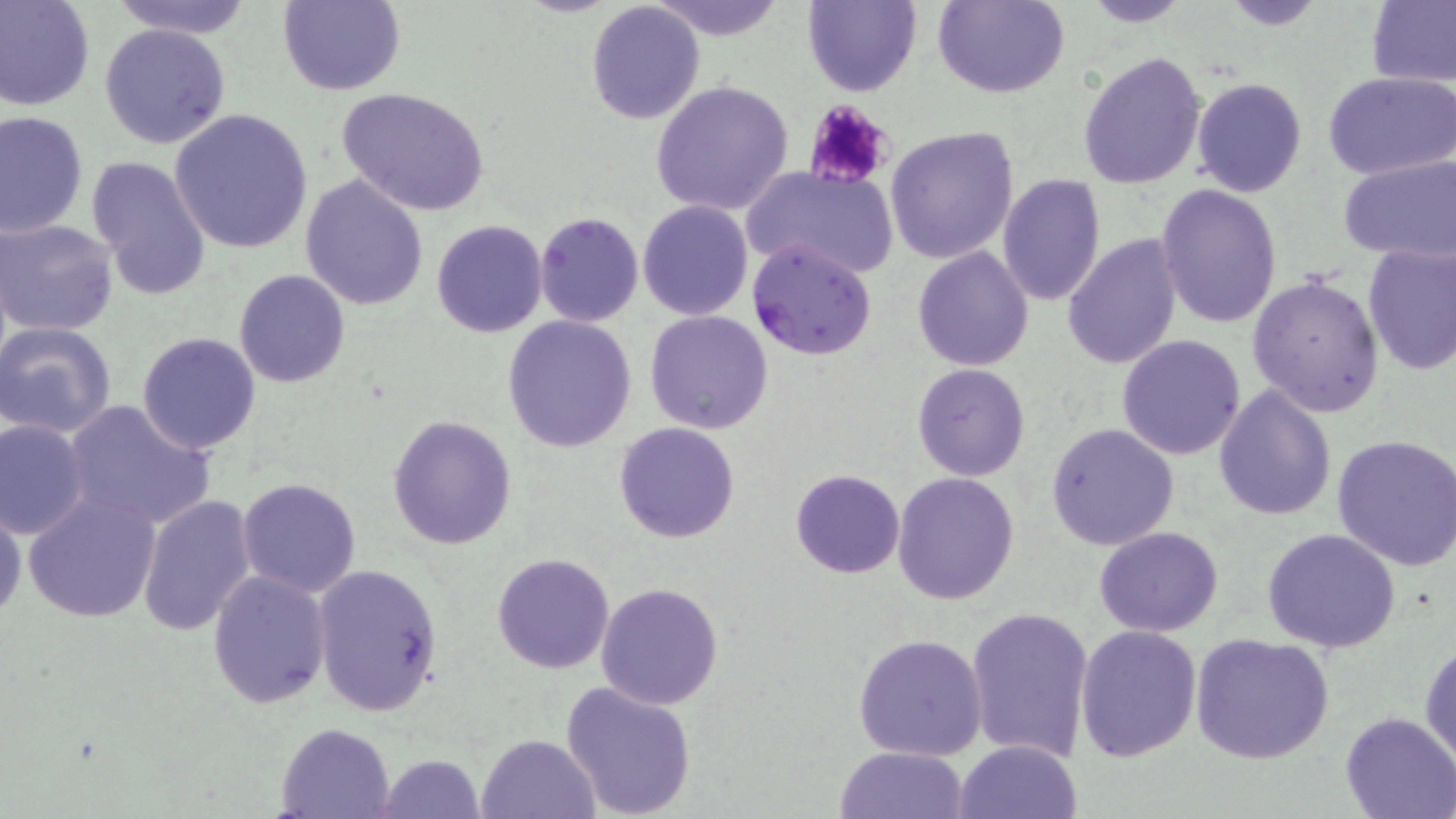

slide-level diagnosis = Plasmodium falciparum
stain = May-Grünwald-Giemsa
Plasmodium falciparum-infected red blood cell locations = approximate bounding boxes as named x1/y1/x2/y2 corners in pixels: (x1=746, y1=236, x2=877, y2=361)
modality = optical microscopy
preparation = thin blood smear
field of view = one of a larger specimen
uninfected red blood cell locations = approximate bounding boxes as named x1/y1/x2/y2 corners in pixels: (x1=0, y1=0, x2=96, y2=112), (x1=105, y1=0, x2=257, y2=38), (x1=275, y1=0, x2=405, y2=95), (x1=647, y1=0, x2=788, y2=40), (x1=934, y1=0, x2=1068, y2=98), (x1=1218, y1=0, x2=1332, y2=29), (x1=1367, y1=0, x2=1456, y2=88), (x1=802, y1=1, x2=921, y2=96), (x1=1078, y1=1, x2=1194, y2=27), (x1=586, y1=2, x2=706, y2=123), (x1=100, y1=23, x2=230, y2=149), (x1=1077, y1=51, x2=1207, y2=189), (x1=1323, y1=72, x2=1456, y2=180), (x1=1191, y1=77, x2=1307, y2=197), (x1=650, y1=79, x2=795, y2=216), (x1=336, y1=87, x2=490, y2=216), (x1=170, y1=108, x2=313, y2=253), (x1=1, y1=111, x2=88, y2=239), (x1=884, y1=126, x2=1019, y2=265), (x1=87, y1=155, x2=212, y2=299), (x1=1337, y1=155, x2=1456, y2=263), (x1=742, y1=166, x2=897, y2=277), (x1=996, y1=172, x2=1106, y2=306), (x1=300, y1=174, x2=430, y2=311), (x1=1155, y1=183, x2=1282, y2=328), (x1=638, y1=200, x2=753, y2=319), (x1=534, y1=212, x2=645, y2=327), (x1=2, y1=217, x2=119, y2=337), (x1=430, y1=219, x2=548, y2=337), (x1=1063, y1=233, x2=1181, y2=371), (x1=1361, y1=244, x2=1456, y2=375), (x1=913, y1=247, x2=1033, y2=370), (x1=234, y1=270, x2=351, y2=388), (x1=1247, y1=273, x2=1387, y2=418), (x1=644, y1=309, x2=773, y2=434), (x1=504, y1=315, x2=636, y2=452), (x1=0, y1=321, x2=118, y2=438), (x1=137, y1=331, x2=261, y2=454), (x1=1117, y1=335, x2=1246, y2=460), (x1=912, y1=363, x2=1031, y2=481), (x1=1213, y1=384, x2=1337, y2=522), (x1=63, y1=402, x2=215, y2=530), (x1=387, y1=416, x2=516, y2=549), (x1=0, y1=417, x2=90, y2=539), (x1=613, y1=421, x2=740, y2=543), (x1=1046, y1=423, x2=1180, y2=550), (x1=1332, y1=434, x2=1456, y2=573), (x1=791, y1=469, x2=905, y2=578), (x1=893, y1=473, x2=1019, y2=607), (x1=237, y1=477, x2=363, y2=598), (x1=22, y1=491, x2=161, y2=623), (x1=136, y1=494, x2=257, y2=636), (x1=0, y1=503, x2=25, y2=621), (x1=1094, y1=525, x2=1224, y2=637), (x1=1261, y1=527, x2=1401, y2=652), (x1=492, y1=553, x2=615, y2=674), (x1=310, y1=562, x2=443, y2=716), (x1=207, y1=569, x2=332, y2=708), (x1=595, y1=581, x2=723, y2=709), (x1=966, y1=606, x2=1094, y2=764), (x1=1074, y1=623, x2=1202, y2=761), (x1=853, y1=632, x2=989, y2=760), (x1=1190, y1=632, x2=1334, y2=765), (x1=1420, y1=637, x2=1455, y2=766), (x1=561, y1=680, x2=697, y2=818), (x1=1338, y1=711, x2=1455, y2=819), (x1=275, y1=721, x2=399, y2=818), (x1=476, y1=733, x2=601, y2=819), (x1=953, y1=739, x2=1083, y2=819), (x1=835, y1=746, x2=968, y2=819), (x1=375, y1=753, x2=485, y2=818)
magnification = 1000x
platelet locations = approximate bounding boxes as named x1/y1/x2/y2 corners in pixels: (x1=802, y1=100, x2=894, y2=189)
image size = 1456×819 pixels